Identify the blood parasite species.
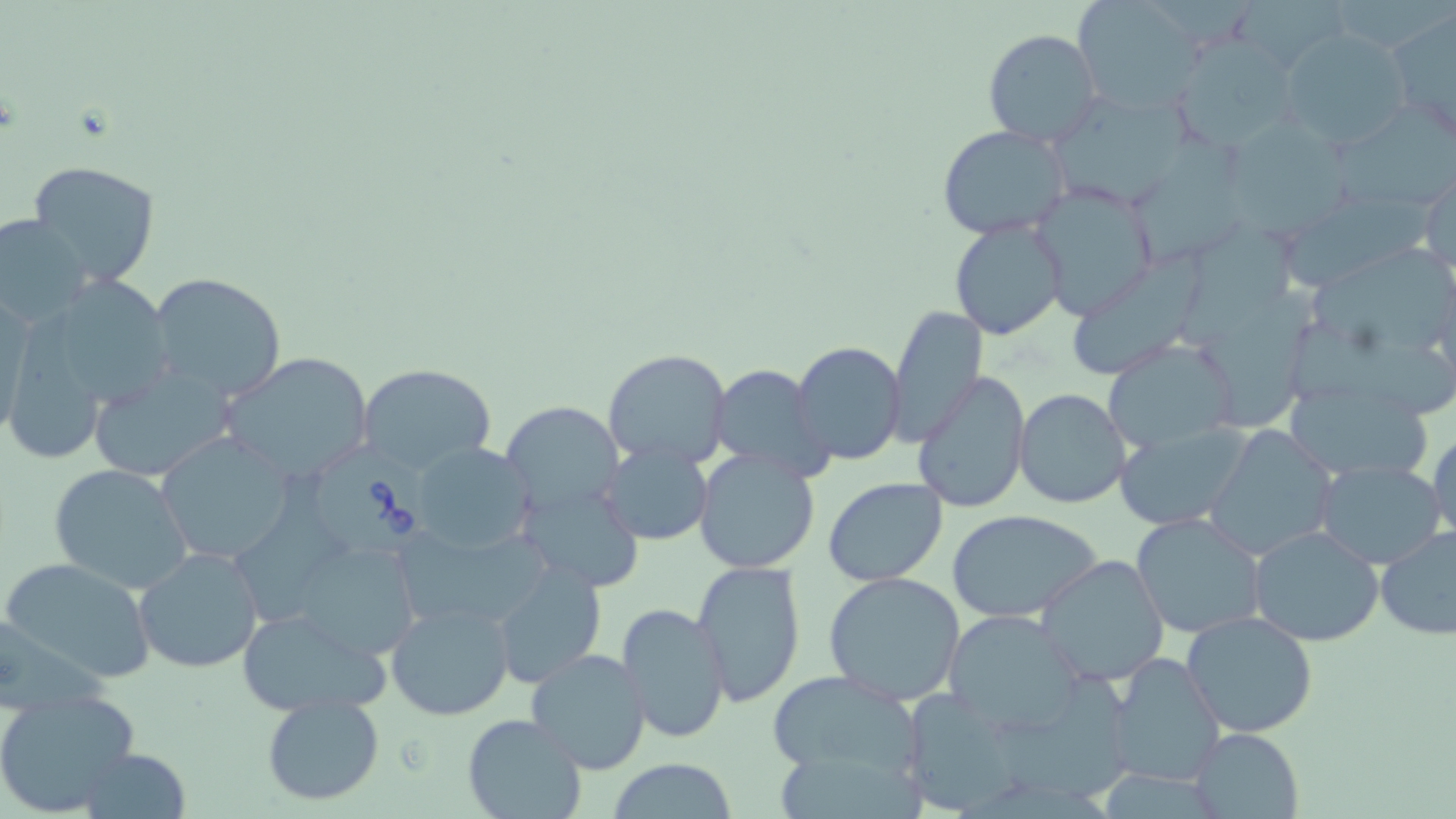

Babesia divergens.

Summary:
  - Coordinate format: approximate bounding boxes as (x1, y1, x2, y2) in pixels
  - Babesia divergens-infected red blood cell locations: (316, 446, 448, 562)
  - Uninfected red blood cell locations: (1072, 0, 1204, 115), (1385, 8, 1456, 142), (983, 29, 1101, 147), (1279, 29, 1412, 150), (1180, 35, 1307, 154), (1055, 92, 1207, 202), (1338, 102, 1456, 209), (1229, 119, 1355, 244), (939, 125, 1070, 240), (1131, 131, 1252, 265), (26, 160, 162, 288), (1419, 167, 1455, 276), (1030, 182, 1158, 321), (1283, 189, 1439, 294), (0, 214, 93, 329), (949, 217, 1068, 339), (1179, 219, 1308, 350), (1071, 245, 1216, 379), (1310, 251, 1456, 350), (146, 272, 291, 401), (30, 277, 177, 413), (1200, 288, 1322, 436), (2, 290, 36, 442), (886, 306, 987, 447), (1299, 323, 1456, 418), (1104, 340, 1239, 454), (791, 341, 905, 464), (602, 347, 733, 469), (218, 349, 375, 484), (87, 362, 238, 483), (357, 362, 496, 475), (710, 364, 832, 479), (913, 371, 1031, 515), (1282, 378, 1436, 483), (1014, 388, 1131, 509), (501, 400, 623, 519), (1113, 424, 1252, 531), (1203, 425, 1338, 560), (1429, 425, 1456, 549), (155, 432, 296, 565), (409, 440, 537, 555), (598, 441, 713, 547), (692, 450, 820, 574), (1312, 458, 1447, 570), (48, 463, 194, 595), (822, 476, 948, 586), (518, 486, 642, 590), (945, 507, 1105, 623), (1132, 512, 1266, 640), (1249, 524, 1385, 646), (272, 525, 432, 666), (1373, 525, 1456, 642), (134, 545, 266, 674), (1036, 553, 1169, 685), (0, 556, 159, 687), (691, 559, 806, 704), (492, 561, 607, 688), (823, 571, 967, 705), (385, 598, 515, 720), (615, 601, 731, 744), (235, 605, 392, 717), (940, 606, 1084, 735), (1181, 611, 1319, 737), (525, 649, 653, 774), (1105, 651, 1227, 788), (767, 669, 923, 773), (0, 690, 140, 817), (261, 692, 384, 807), (462, 712, 585, 819), (1188, 727, 1306, 819), (78, 747, 191, 817), (607, 757, 737, 819)
  - Magnification: 1000x
  - Stain: May-Grünwald-Giemsa
  - Modality: optical microscopy
  - Image size: 1456×819 pixels
  - Field of view: one of a larger specimen
  - Preparation: thin blood smear